Locate every blood parasite and identify its species.
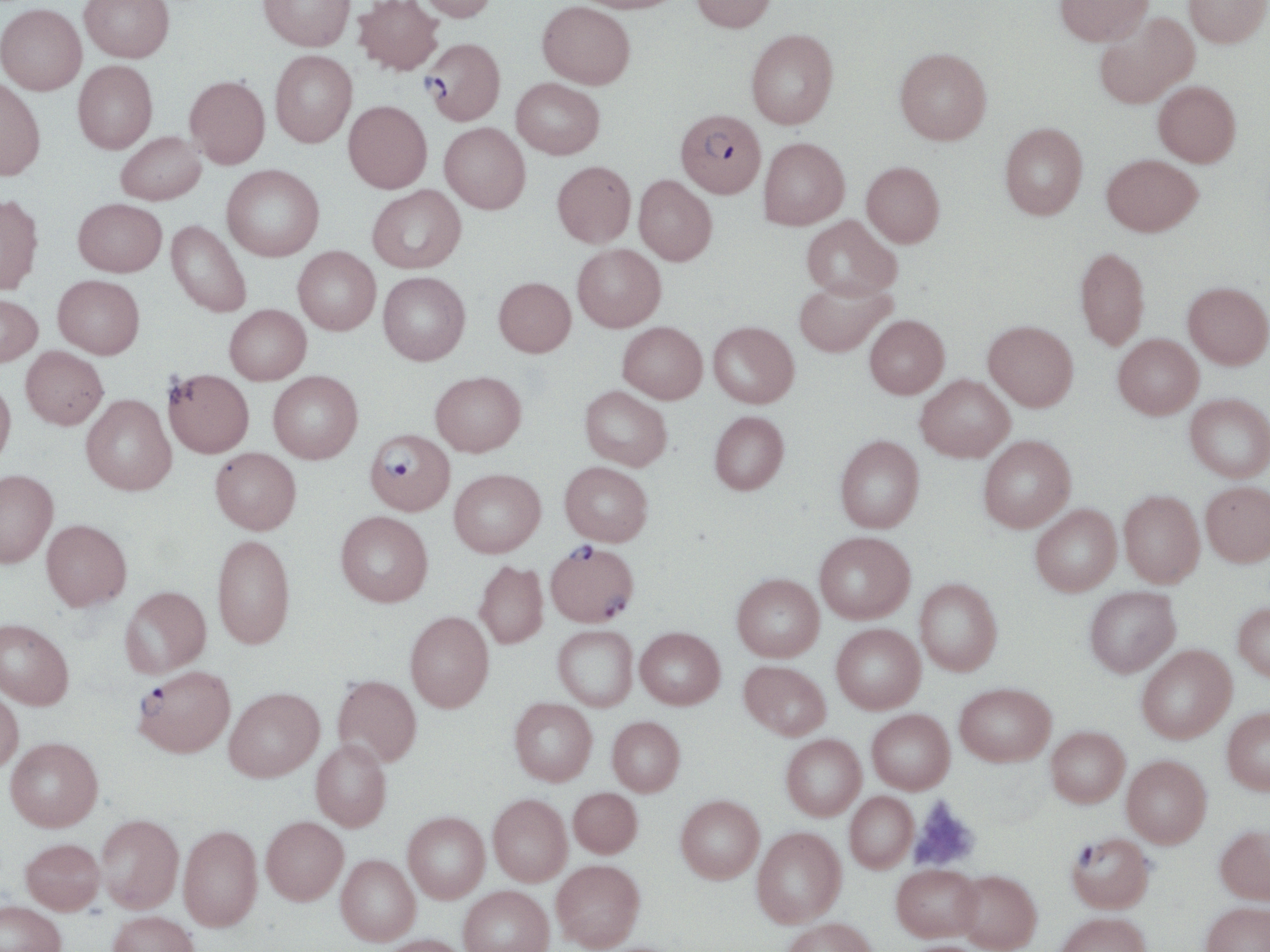
Approximate bounding boxes as named x1/y1/x2/y2 corners in pixels.
Plasmodium falciparum-infected red blood cells: (x1=423, y1=38, x2=506, y2=125), (x1=675, y1=109, x2=766, y2=198), (x1=364, y1=430, x2=455, y2=513), (x1=546, y1=542, x2=639, y2=626), (x1=133, y1=665, x2=236, y2=757), (x1=1067, y1=832, x2=1155, y2=913).
No Plasmodium ovale, Plasmodium malariae, Plasmodium vivax, Babesia divergens, or Trypanosoma brucei observed.

Summary:
  - Uninfected red blood cell locations: (x1=80, y1=0, x2=174, y2=62), (x1=353, y1=0, x2=444, y2=75), (x1=415, y1=0, x2=498, y2=22), (x1=572, y1=0, x2=685, y2=13), (x1=691, y1=0, x2=776, y2=32), (x1=1054, y1=0, x2=1153, y2=46), (x1=1184, y1=0, x2=1270, y2=47), (x1=258, y1=1, x2=356, y2=51), (x1=537, y1=1, x2=635, y2=89), (x1=0, y1=3, x2=87, y2=94), (x1=1094, y1=11, x2=1199, y2=108), (x1=746, y1=29, x2=838, y2=129), (x1=894, y1=47, x2=991, y2=145), (x1=270, y1=51, x2=357, y2=148), (x1=73, y1=61, x2=157, y2=153), (x1=185, y1=76, x2=270, y2=169), (x1=0, y1=78, x2=45, y2=181), (x1=511, y1=78, x2=605, y2=159), (x1=1153, y1=81, x2=1241, y2=167), (x1=344, y1=101, x2=432, y2=193), (x1=1000, y1=122, x2=1088, y2=220), (x1=440, y1=123, x2=530, y2=214), (x1=116, y1=131, x2=206, y2=205), (x1=759, y1=137, x2=849, y2=230), (x1=1102, y1=154, x2=1203, y2=236), (x1=552, y1=161, x2=636, y2=247), (x1=861, y1=161, x2=944, y2=247), (x1=222, y1=164, x2=324, y2=261), (x1=634, y1=175, x2=717, y2=265), (x1=367, y1=185, x2=465, y2=273), (x1=0, y1=195, x2=43, y2=295), (x1=73, y1=198, x2=167, y2=277), (x1=801, y1=215, x2=901, y2=300), (x1=166, y1=220, x2=252, y2=318), (x1=572, y1=244, x2=666, y2=332), (x1=293, y1=246, x2=380, y2=335), (x1=1075, y1=247, x2=1150, y2=351), (x1=378, y1=271, x2=470, y2=365), (x1=53, y1=275, x2=145, y2=359), (x1=494, y1=277, x2=575, y2=357), (x1=794, y1=279, x2=895, y2=357), (x1=1183, y1=281, x2=1270, y2=369), (x1=0, y1=293, x2=42, y2=367), (x1=224, y1=304, x2=311, y2=384), (x1=865, y1=315, x2=949, y2=398), (x1=983, y1=320, x2=1078, y2=411), (x1=618, y1=321, x2=708, y2=403), (x1=709, y1=321, x2=799, y2=407), (x1=1113, y1=334, x2=1203, y2=419), (x1=21, y1=346, x2=107, y2=429), (x1=163, y1=368, x2=253, y2=457), (x1=431, y1=370, x2=526, y2=456), (x1=268, y1=371, x2=363, y2=463), (x1=916, y1=374, x2=1014, y2=461), (x1=0, y1=378, x2=16, y2=468), (x1=580, y1=385, x2=672, y2=471), (x1=1185, y1=393, x2=1270, y2=482), (x1=81, y1=394, x2=176, y2=495), (x1=709, y1=411, x2=789, y2=494), (x1=835, y1=435, x2=924, y2=532), (x1=978, y1=435, x2=1076, y2=532), (x1=210, y1=447, x2=301, y2=534), (x1=560, y1=461, x2=653, y2=545), (x1=449, y1=469, x2=545, y2=557), (x1=0, y1=470, x2=58, y2=567), (x1=1201, y1=482, x2=1270, y2=566), (x1=1119, y1=490, x2=1204, y2=587), (x1=1030, y1=505, x2=1121, y2=596), (x1=336, y1=511, x2=433, y2=606), (x1=41, y1=519, x2=131, y2=610), (x1=814, y1=532, x2=915, y2=623), (x1=212, y1=534, x2=295, y2=649), (x1=474, y1=561, x2=548, y2=649), (x1=732, y1=574, x2=824, y2=661), (x1=915, y1=578, x2=1002, y2=675), (x1=121, y1=586, x2=211, y2=677), (x1=1084, y1=587, x2=1180, y2=677), (x1=1233, y1=603, x2=1270, y2=681), (x1=405, y1=612, x2=494, y2=712), (x1=0, y1=618, x2=74, y2=710), (x1=831, y1=624, x2=925, y2=714), (x1=553, y1=626, x2=638, y2=711), (x1=635, y1=627, x2=725, y2=709), (x1=1137, y1=645, x2=1236, y2=742), (x1=740, y1=661, x2=831, y2=740), (x1=333, y1=675, x2=422, y2=767), (x1=955, y1=683, x2=1055, y2=765), (x1=0, y1=687, x2=23, y2=773), (x1=224, y1=687, x2=324, y2=781), (x1=509, y1=697, x2=597, y2=786), (x1=1222, y1=707, x2=1270, y2=794), (x1=867, y1=710, x2=955, y2=794), (x1=607, y1=716, x2=685, y2=795), (x1=1047, y1=727, x2=1129, y2=807), (x1=781, y1=735, x2=866, y2=820), (x1=5, y1=736, x2=103, y2=831), (x1=311, y1=740, x2=391, y2=831), (x1=1122, y1=755, x2=1211, y2=847), (x1=569, y1=787, x2=642, y2=857), (x1=845, y1=792, x2=917, y2=872), (x1=488, y1=794, x2=572, y2=885), (x1=676, y1=795, x2=764, y2=883), (x1=403, y1=812, x2=490, y2=903), (x1=96, y1=814, x2=183, y2=913), (x1=261, y1=816, x2=348, y2=905), (x1=178, y1=824, x2=263, y2=932), (x1=1215, y1=826, x2=1270, y2=903), (x1=752, y1=827, x2=846, y2=927), (x1=21, y1=838, x2=105, y2=914), (x1=336, y1=854, x2=420, y2=945), (x1=551, y1=860, x2=645, y2=951), (x1=891, y1=864, x2=982, y2=941), (x1=954, y1=870, x2=1041, y2=952), (x1=458, y1=885, x2=554, y2=952), (x1=0, y1=900, x2=66, y2=952), (x1=1201, y1=902, x2=1270, y2=952), (x1=108, y1=911, x2=199, y2=952), (x1=1052, y1=912, x2=1151, y2=952), (x1=781, y1=917, x2=879, y2=952), (x1=378, y1=934, x2=469, y2=952)
  - Platelet locations: (x1=909, y1=796, x2=980, y2=873)
  - Slide-level diagnosis: Plasmodium falciparum
  - Image size: 1270×952 pixels
  - Modality: light microscopy
  - Stain: May-Grünwald-Giemsa
  - Preparation: thin blood smear
  - Magnification: 1000x
  - Field of view: one of a larger specimen